Assess this cell for malaria.
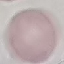

It is uninfected.

Summary:
  - Capture: smartphone through the microscope eyepiece
  - Stain: Giemsa
  - Image type: cell patch, automatically extracted from a larger field of view and resized to 64 × 64 pixels
  - Preparation: thin smear